Locate every malaria parasite.
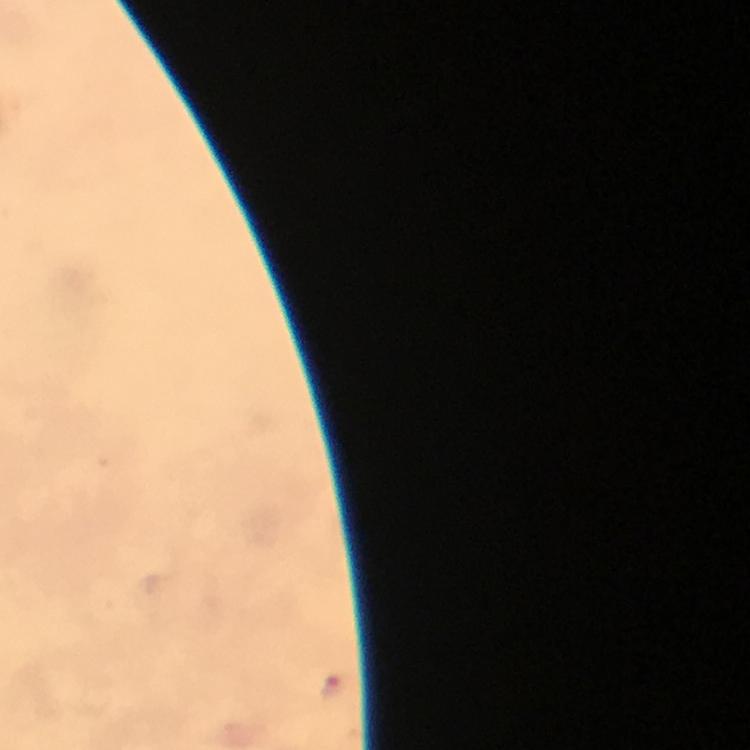
Approximate object centers, in pixels from the top-left corner.
Malaria parasites: (x=335, y=686).

At 100x magnification. Cropped region of a single field of view. Image is 750×750 pixels. Giemsa stain. From a malaria diagnostic workup. Immersion oil applied. Thick blood smear. Photographed with a smartphone mounted on the microscope.